Locate the P. falciparum-infected red blood cells and any of indeterminate infection status.
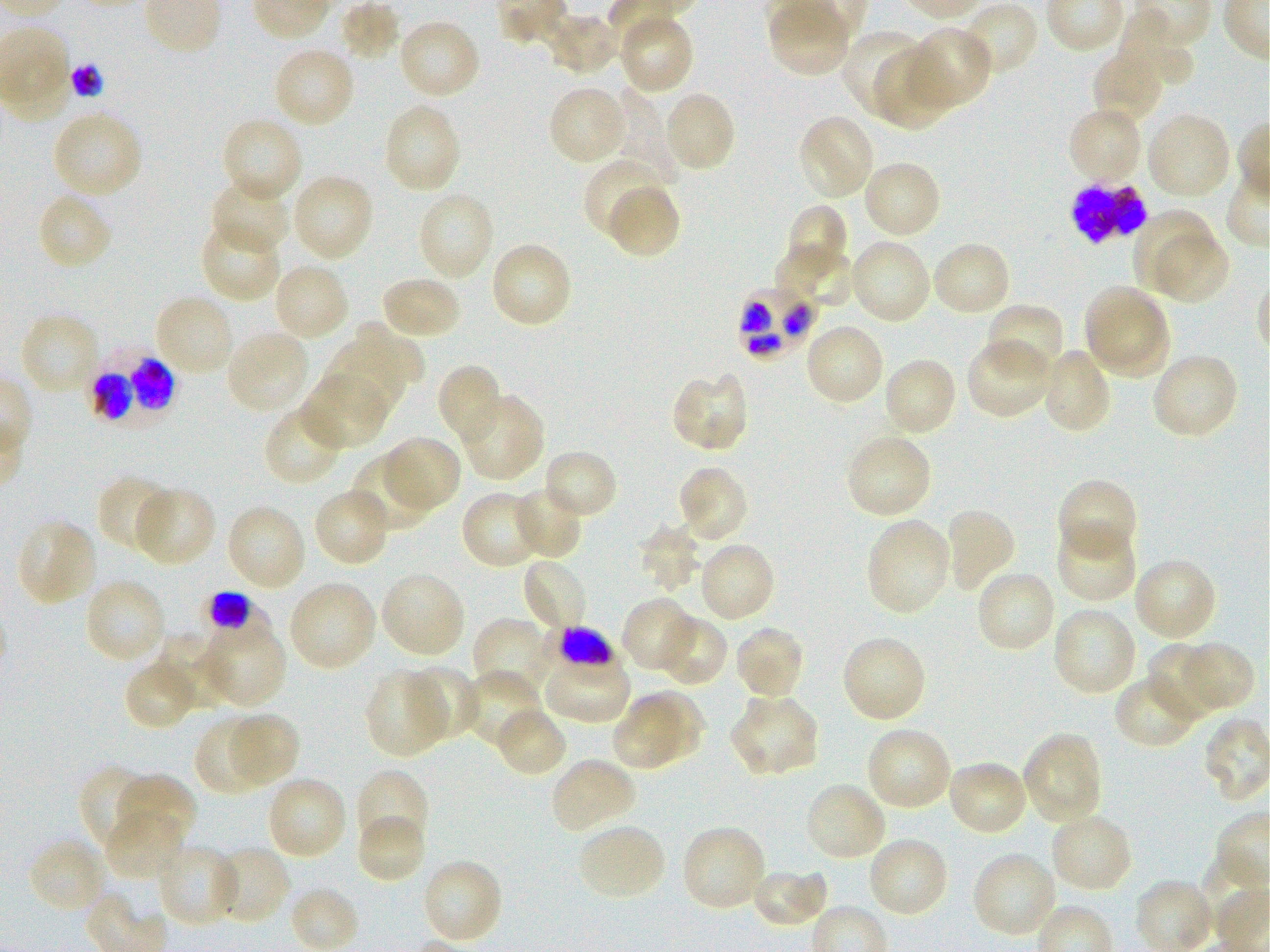

Approximate bounding boxes as {x1, y1, x2, y2} in pixels. Not every red blood cell is marked. A life-cycle stage — or a range of stages, where the recorded stages span more than one — follows each staged infected red blood cell.
Infected red blood cells: {1071, 178, 1152, 245}; {738, 286, 814, 361}; {87, 345, 184, 429}; {197, 594, 273, 657} early trophozoite to late schizont; {540, 629, 617, 683}.
No red blood cells of indeterminate infection status observed.

Locations of uninfected red blood cells: {618, 13, 695, 95}, {397, 18, 481, 100}, {905, 26, 992, 111}, {840, 27, 927, 116}, {272, 47, 355, 129}, {1091, 50, 1164, 125}, {873, 52, 957, 130}, {548, 85, 629, 167}, {619, 89, 683, 184}, {663, 91, 736, 174}, {383, 102, 462, 194}, {1067, 106, 1144, 185}, {51, 111, 143, 199}, {1147, 111, 1232, 200}, {797, 115, 876, 201}, {220, 117, 304, 204}, {582, 156, 665, 241}, {861, 160, 943, 240}, {291, 173, 375, 262}, {209, 178, 290, 257}, {606, 183, 681, 260}, {415, 190, 495, 281}, {36, 192, 114, 272}, {784, 203, 849, 276}, {1132, 211, 1216, 292}, {199, 221, 282, 304}, {1155, 231, 1231, 303}, {849, 238, 931, 326}, {930, 240, 1013, 318}, {489, 241, 575, 330}, {773, 243, 855, 312}, {273, 262, 350, 340}, {380, 274, 463, 340}, {1085, 287, 1162, 362}, {153, 294, 235, 378}, {1090, 300, 1172, 379}, {986, 302, 1065, 380}, {20, 313, 99, 398}, {322, 321, 427, 404}, {804, 322, 885, 406}, {226, 330, 310, 414}, {965, 337, 1051, 419}, {1038, 347, 1112, 435}, {1151, 353, 1240, 441}, {882, 356, 957, 437}, {436, 364, 503, 447}, {303, 372, 390, 450}, {670, 372, 750, 454}, {458, 392, 545, 482}, {263, 405, 344, 487}, {845, 433, 932, 520}, {382, 435, 463, 512}, {541, 449, 619, 521}, {352, 454, 435, 533}, {676, 466, 749, 544}, {97, 474, 175, 552}, {1056, 478, 1139, 564}, {134, 486, 216, 567}, {511, 486, 584, 561}, {312, 487, 391, 568}, {460, 490, 542, 570}, {225, 503, 308, 592}, {942, 506, 1017, 594}, {16, 518, 97, 608}, {865, 519, 952, 616}, {1054, 522, 1138, 604}, {638, 523, 702, 593}, {697, 542, 776, 623}, {1132, 556, 1219, 641}, {520, 557, 590, 633}, {975, 569, 1057, 654}, {379, 571, 467, 659}, {83, 578, 167, 665}, {287, 579, 379, 672}, {621, 597, 696, 673}, {1051, 606, 1138, 697}, {657, 613, 729, 688}, {474, 617, 555, 700}, {734, 624, 806, 701}, {163, 631, 232, 709}, {204, 634, 289, 711}, {841, 635, 927, 723}, {1180, 641, 1256, 713}, {1147, 642, 1220, 719}, {542, 650, 630, 724}, {122, 659, 197, 732}, {402, 664, 480, 741}, {364, 669, 448, 759}, {465, 669, 543, 749}, {1114, 674, 1197, 750}, {634, 689, 707, 757}, {614, 693, 681, 767}, {729, 693, 820, 777}, {494, 707, 569, 780}, {228, 712, 302, 786}, {193, 715, 273, 796}, {866, 726, 952, 811}, {1022, 732, 1104, 826}, {550, 756, 637, 835}, {946, 759, 1030, 838}, {80, 764, 154, 854}, {355, 769, 430, 849}, {119, 772, 196, 851}, {265, 776, 348, 861}, {804, 781, 887, 863}, {102, 809, 184, 881}, {1049, 812, 1133, 894}, {356, 813, 426, 885}, {577, 823, 666, 902}, {681, 825, 768, 912}, {866, 836, 950, 919}, {28, 837, 109, 914}, {156, 843, 240, 927}, {213, 844, 292, 926}, {971, 851, 1058, 939}, {421, 856, 503, 946}, {749, 865, 830, 929}. Giemsa stain. Thin blood film. 100x objective under oil immersion, numerical aperture 1.25. One field from this slide. Donor blood group O+. Image is 1270×952 pixels. P. falciparum strain 3D7 maintained in static in-vitro culture.